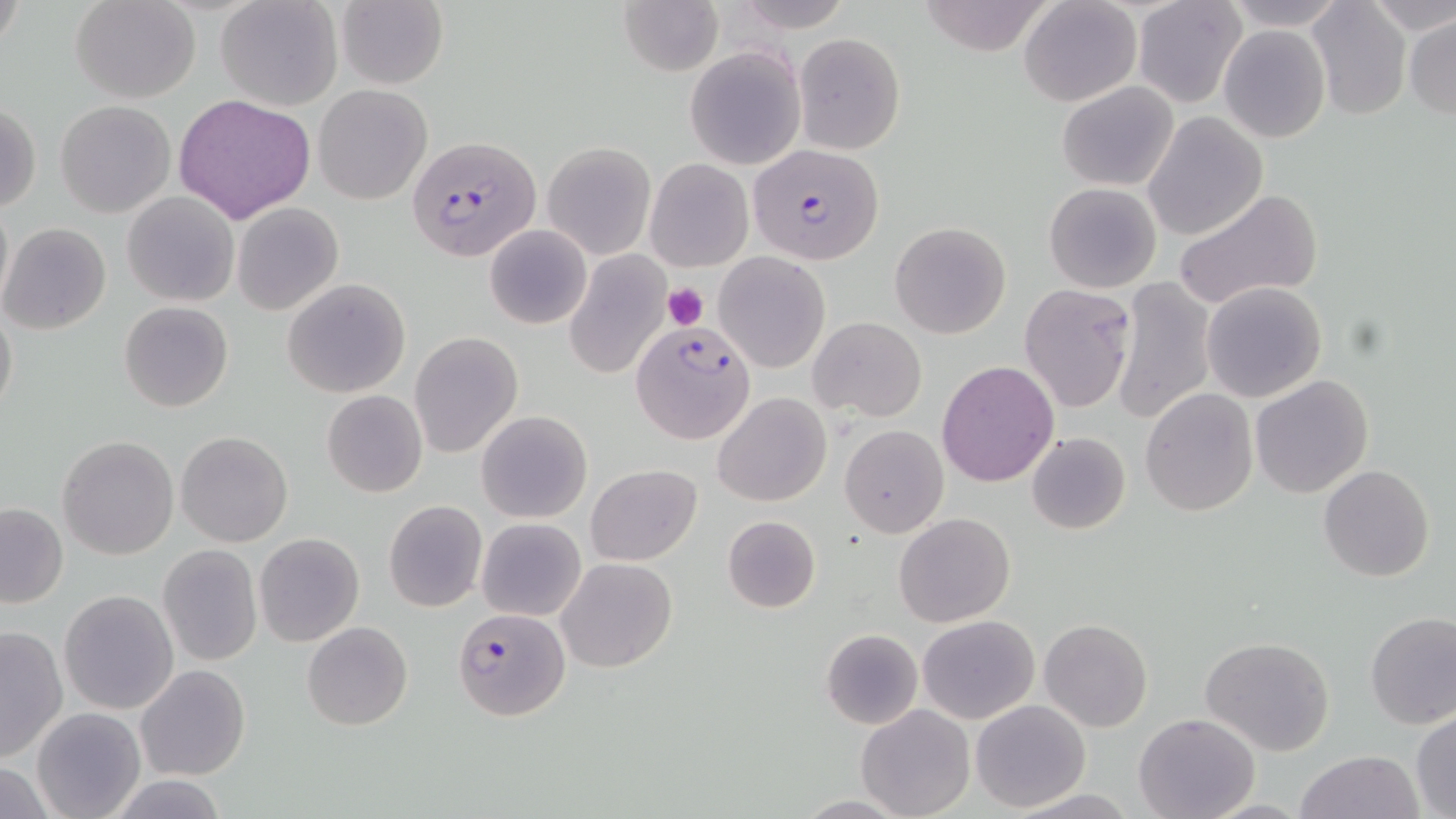

Summary:
  - Coordinate format: approximate bounding boxes as [x1, y1, x2, y2] in pixels
  - Uninfected red blood cell locations: [70, 0, 201, 102], [215, 0, 341, 111], [337, 0, 449, 89], [617, 0, 722, 76], [729, 0, 854, 31], [917, 0, 1059, 57], [1018, 0, 1143, 106], [1219, 0, 1350, 31], [1306, 0, 1410, 121], [1363, 0, 1455, 33], [1132, 1, 1246, 109], [1405, 14, 1455, 118], [1219, 24, 1330, 144], [794, 33, 904, 154], [684, 45, 807, 170], [1057, 81, 1180, 190], [314, 84, 431, 204], [174, 93, 315, 223], [56, 100, 175, 218], [1, 105, 41, 213], [1143, 112, 1269, 240], [541, 141, 655, 260], [645, 158, 752, 272], [1044, 183, 1161, 292], [1172, 189, 1322, 315], [122, 192, 239, 307], [0, 195, 12, 308], [231, 202, 344, 315], [1, 221, 112, 335], [889, 221, 1011, 339], [484, 224, 591, 330], [715, 252, 829, 372], [563, 253, 669, 380], [1111, 275, 1216, 426], [283, 278, 410, 398], [1200, 283, 1326, 403], [1019, 284, 1137, 414], [119, 301, 234, 413], [1, 303, 18, 419], [809, 317, 926, 421], [411, 332, 523, 458], [936, 359, 1059, 487], [1251, 375, 1374, 499], [1139, 388, 1257, 516], [321, 390, 428, 497], [713, 392, 831, 508], [477, 410, 593, 523], [840, 425, 948, 537], [175, 430, 293, 547], [1026, 431, 1131, 534], [58, 436, 179, 559], [586, 465, 701, 564], [1319, 465, 1436, 583], [384, 500, 487, 613], [0, 502, 67, 607], [894, 512, 1016, 626], [721, 514, 820, 614], [477, 519, 586, 620], [253, 533, 364, 646], [158, 545, 263, 666], [557, 557, 675, 672], [59, 589, 178, 715], [1365, 613, 1456, 730], [917, 614, 1040, 723], [1039, 619, 1152, 732], [302, 620, 413, 730], [0, 626, 67, 763], [820, 628, 923, 730], [1199, 636, 1336, 756], [135, 664, 250, 782], [970, 700, 1089, 812], [856, 704, 976, 819], [31, 707, 145, 819], [1410, 709, 1456, 817], [1133, 713, 1259, 819], [1296, 749, 1423, 819], [107, 776, 231, 817], [1000, 788, 1145, 818], [793, 794, 913, 817]
  - Plasmodium falciparum-infected red blood cell locations: [408, 134, 540, 264], [745, 146, 886, 261], [631, 319, 758, 446], [453, 607, 570, 722]
  - Platelet locations: [662, 283, 708, 328]
  - Slide-level diagnosis: Plasmodium falciparum
  - Magnification: 1000x
  - Field of view: one of a larger specimen
  - Stain: May-Grünwald-Giemsa
  - Preparation: thin blood film
  - Image size: 1456×819 pixels
  - Modality: light microscopy